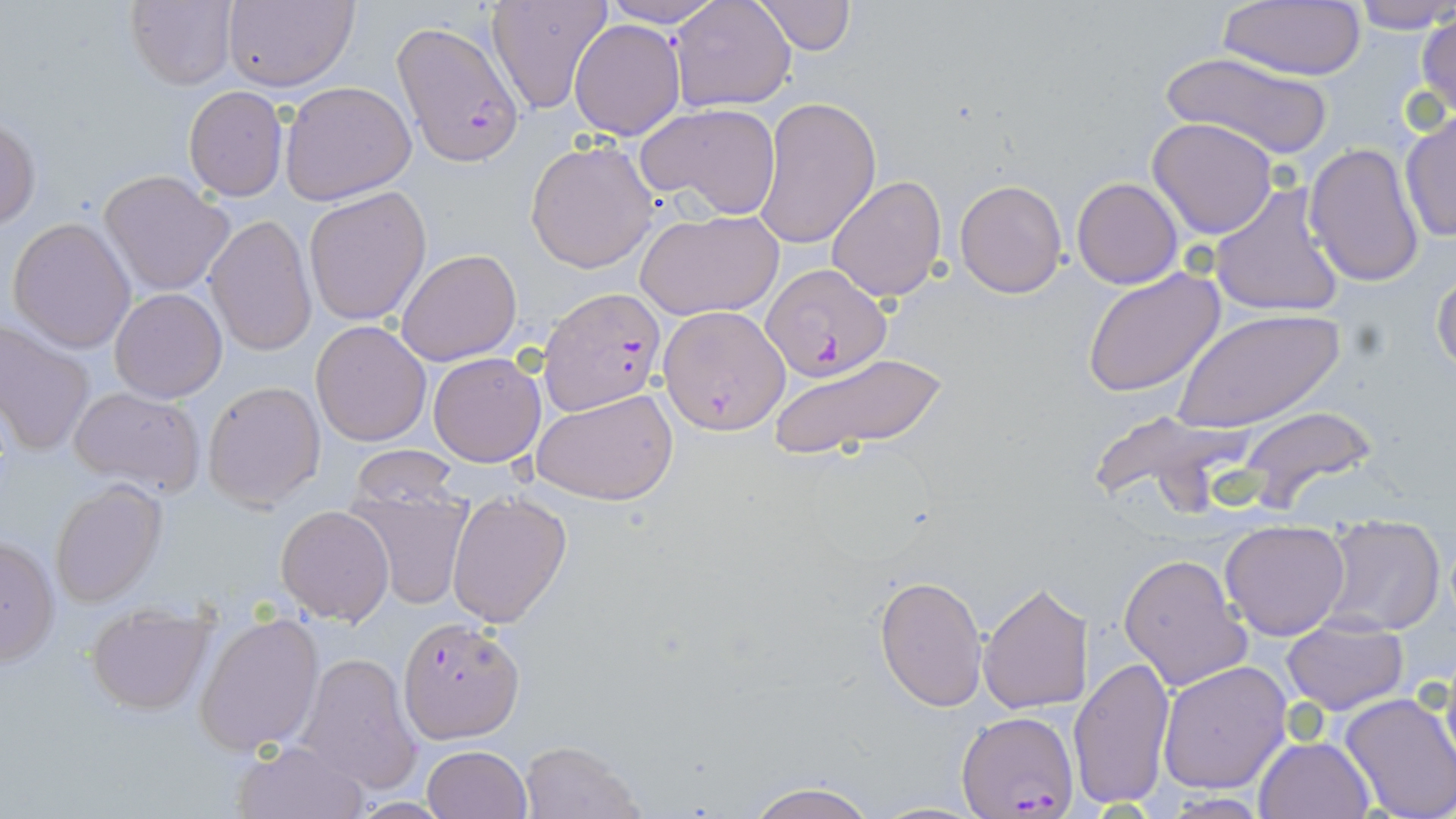 Approximate bounding boxes as (x1, y1, x2, y2) in pixels. Plasmodium falciparum-infected red blood cell locations: (394, 22, 523, 166), (761, 265, 890, 383), (541, 286, 661, 415), (658, 304, 788, 433), (396, 617, 523, 744), (956, 712, 1076, 817). Uninfected red blood cell locations: (598, 0, 729, 28), (670, 0, 797, 112), (1351, 0, 1456, 35), (123, 1, 239, 89), (221, 1, 357, 90), (485, 1, 610, 112), (756, 1, 853, 55), (1218, 3, 1368, 80), (1414, 10, 1456, 124), (568, 19, 686, 139), (1157, 51, 1336, 162), (280, 80, 417, 206), (183, 85, 288, 201), (754, 96, 881, 250), (636, 103, 780, 219), (1398, 110, 1455, 243), (1, 115, 39, 232), (1147, 118, 1278, 239), (525, 140, 657, 272), (1305, 141, 1425, 290), (100, 170, 234, 297), (827, 174, 947, 302), (1072, 176, 1183, 289), (954, 178, 1068, 299), (1210, 182, 1348, 320), (303, 185, 432, 326), (635, 208, 783, 319), (205, 214, 317, 358), (7, 217, 137, 353), (395, 248, 522, 365), (1431, 264, 1456, 381), (1081, 267, 1227, 396), (109, 288, 228, 403), (1173, 308, 1343, 432), (0, 319, 95, 457), (310, 320, 432, 447), (427, 352, 546, 466), (771, 352, 949, 459), (201, 380, 327, 509), (65, 385, 205, 496), (532, 387, 679, 506), (1238, 404, 1378, 512), (1083, 406, 1249, 516), (349, 444, 462, 511), (50, 480, 166, 608), (344, 482, 476, 610), (445, 491, 571, 629), (275, 504, 394, 625), (1318, 512, 1447, 637), (1219, 519, 1350, 639), (0, 535, 62, 669), (1119, 553, 1255, 692), (874, 573, 988, 712), (978, 581, 1094, 715), (84, 602, 216, 715), (194, 613, 324, 754), (1282, 619, 1408, 714), (293, 652, 421, 794), (1068, 657, 1176, 810), (1157, 660, 1294, 793), (1340, 693, 1456, 819), (1255, 736, 1374, 819), (232, 738, 369, 819), (519, 741, 644, 819), (422, 746, 532, 819), (743, 778, 878, 819). Slide-level diagnosis: Plasmodium falciparum. One field of a larger specimen. Captured at 1000x magnification. Light microscopy. Thin blood smear. Image is 1456×819 pixels. May-Grünwald-Giemsa stain.